Look for Plasmodium parasites.
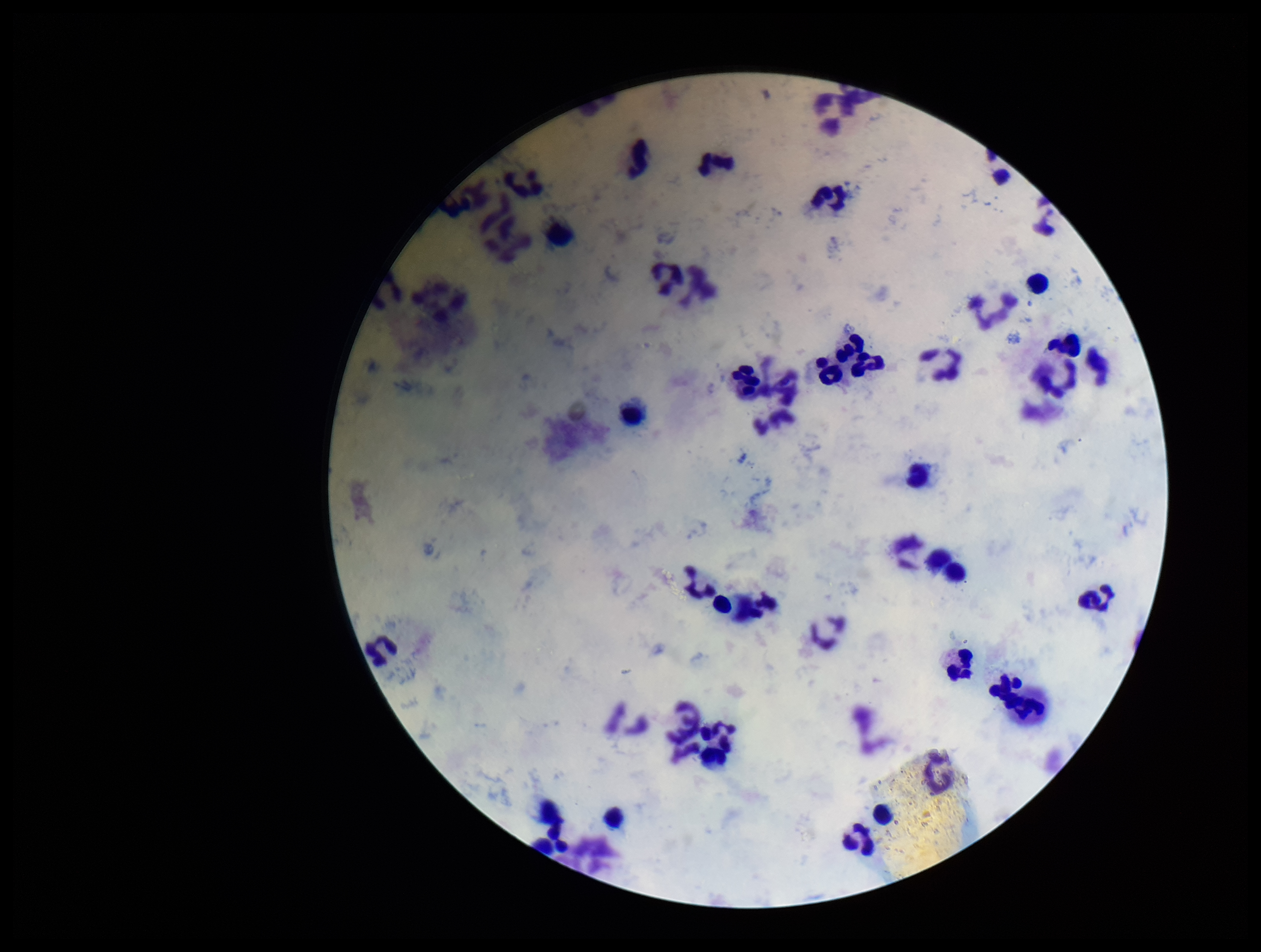

None seen.

Summary:
  - Patient malaria status: negative
  - Stain: Giemsa
  - Image size: 1261×952 pixels
  - Capture: smartphone photograph through the microscope eyepiece
  - Preparation: thick smear
  - Field of view: one from this slide
  - Leukocyte count: 42
  - Parasite count: 0